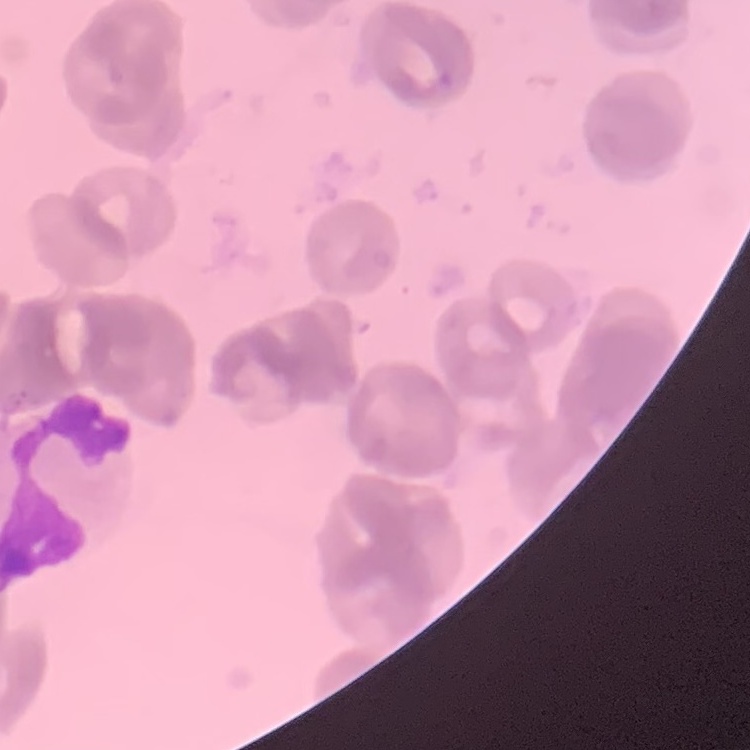

Summary:
  - Red blood cell morphology: rouleaux formation
  - Stain: Field's or Giemsa
  - Image type: one tile cut from a larger photomicrograph
  - Preparation: thin blood smear